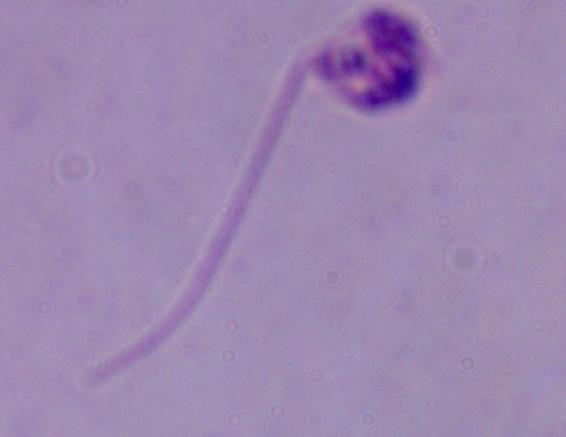
{
  "modality": "micrograph",
  "identification": "Leishmania",
  "magnification": "1000x"
}